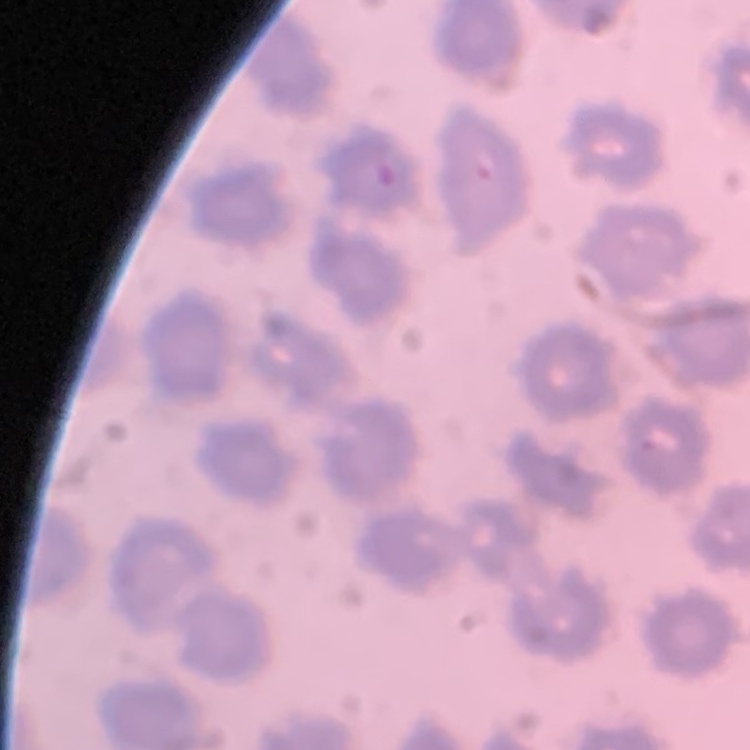

erythrocyte morphology = no rouleaux formation
stain = Field's or Giemsa
image type = square crop of a larger photomicrograph
preparation = thin blood smear